Point out cells.
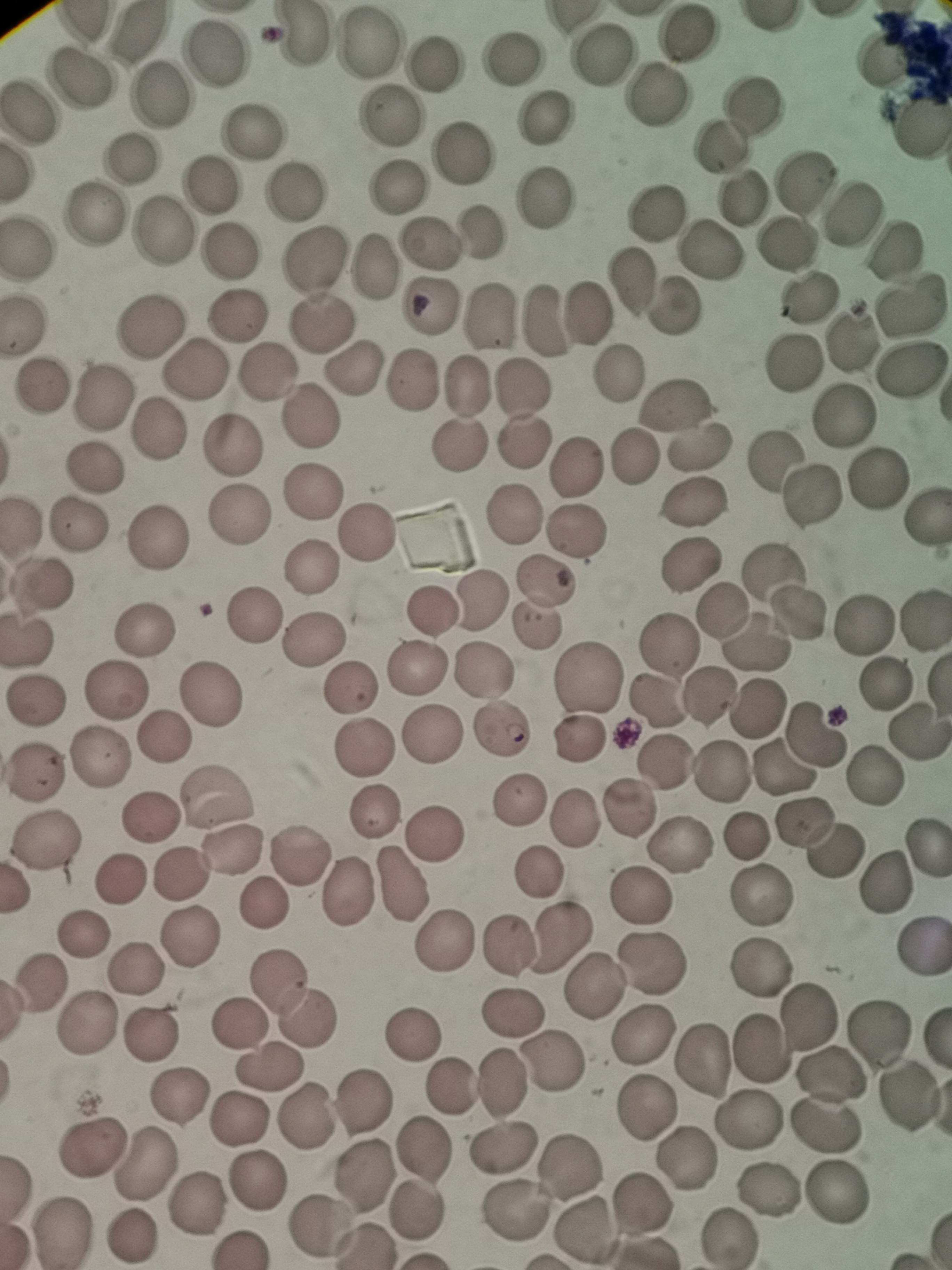

Approximate centers as (x, y) in pixels.
Cells: (689, 33), (302, 34), (372, 42), (218, 52), (516, 53), (601, 54), (440, 62), (79, 79), (161, 94), (659, 97), (752, 102), (30, 111), (389, 116), (547, 119), (920, 124), (255, 130), (721, 145), (467, 152), (133, 158), (805, 181), (212, 183), (397, 187), (296, 189), (549, 196), (745, 197), (852, 211), (96, 212), (654, 212), (162, 227), (482, 233), (429, 242), (786, 245), (228, 247), (27, 248), (714, 250), (894, 250), (314, 262), (375, 266), (634, 282), (808, 300), (676, 303), (910, 304), (429, 306), (237, 312), (589, 312), (489, 318), (545, 321), (153, 322), (23, 323), (322, 324), (847, 339), (795, 361), (357, 367), (911, 367), (195, 369), (265, 371), (620, 372), (413, 382), (466, 387), (42, 388), (519, 390), (105, 396), (675, 404), (842, 414), (310, 419), (158, 429), (523, 441), (236, 445), (701, 445), (461, 447), (631, 456), (773, 463), (578, 466), (94, 467), (876, 478), (315, 488), (812, 496), (693, 501), (514, 514), (243, 516), (925, 519), (78, 524), (576, 531), (366, 532), (158, 537), (691, 564), (310, 566), (775, 566), (545, 579), (40, 586), (484, 600), (725, 608), (434, 611), (798, 613), (255, 616), (923, 620), (534, 625), (868, 627), (144, 630), (28, 637), (314, 640), (754, 642), (665, 646), (485, 667), (419, 668), (586, 676), (884, 684), (348, 688), (117, 689), (708, 692), (214, 693), (36, 700), (656, 703), (757, 709), (501, 730), (917, 733), (815, 734), (163, 735), (437, 736), (580, 737), (363, 748), (102, 757), (665, 761), (783, 767), (720, 772), (35, 775), (873, 777), (221, 799), (524, 800), (632, 808), (375, 812), (573, 815), (152, 818), (801, 822), (436, 825), (748, 836), (47, 841), (680, 845), (836, 851), (927, 851), (234, 853), (299, 854), (537, 873), (179, 876), (120, 880), (882, 883), (399, 885), (349, 895), (761, 896), (641, 897), (261, 905), (83, 933), (564, 936), (189, 938), (444, 939), (506, 945), (920, 949), (652, 961), (761, 968), (137, 969), (279, 979), (596, 983), (38, 987), (511, 1011), (809, 1016), (309, 1018), (88, 1024), (240, 1024), (642, 1030), (876, 1034), (150, 1035), (416, 1035), (702, 1057), (554, 1060), (268, 1068), (833, 1074), (503, 1084), (452, 1085), (180, 1097), (907, 1098), (363, 1101), (647, 1106), (304, 1117), (240, 1120), (749, 1121), (827, 1127), (95, 1144), (504, 1145), (425, 1150), (688, 1159), (146, 1164), (572, 1166), (360, 1175), (256, 1178), (770, 1191), (837, 1196), (198, 1203), (642, 1205), (416, 1210), (517, 1211), (324, 1226), (585, 1230), (62, 1233), (132, 1237), (730, 1239).

Image is 952×1270 pixels. Single field of view. Giemsa-stained preparation. Acquired by smartphone through the microscope eyepiece. Thin smear of blood.